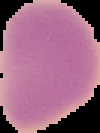

preparation = thin blood film
image type = cell region segmented out of the field of view; surrounding area masked to black
malaria status = uninfected
image size = 100×133 pixels